Locate every P. falciparum parasite and give its life-cycle stage, and locate every leukocyte and any debris.
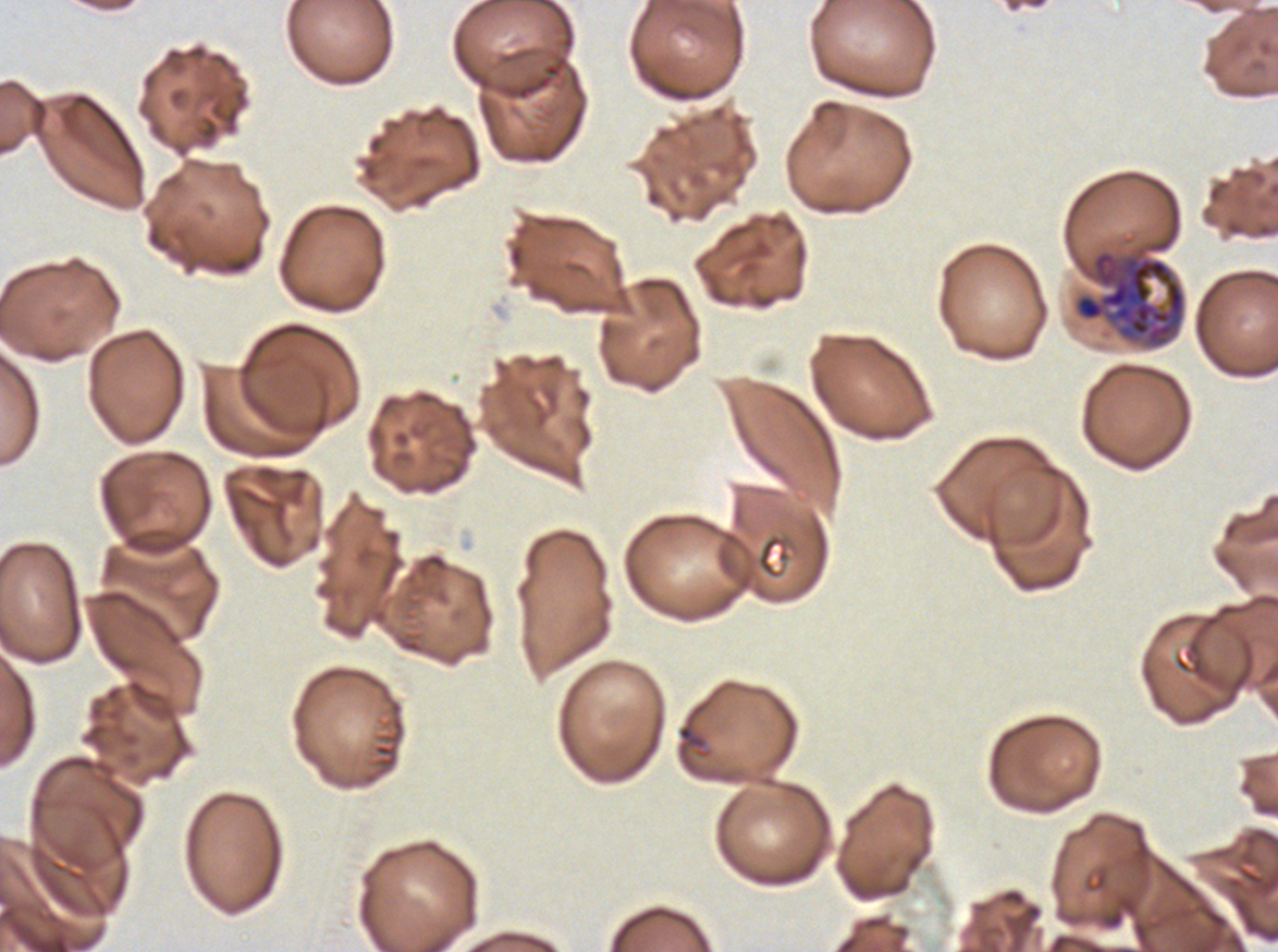

Approximate bounding boxes as [x1, y1, x2, y2] in pixels.
Rings: [677, 723, 707, 751].
Early schizonts: [1074, 250, 1186, 348].
No late-ring/early-trophozoite forms, mid trophozoites, late trophozoites, late schizonts, segmenters, gametocytes, leukocytes, or debris observed.

{
  "image_size": "1278×952 pixels",
  "field_of_view": "one sub-image of a larger composite",
  "stain": "Giemsa",
  "specimen": "P. falciparum from a patient in The Gambia, cultured ex vivo for 24 to 48 hours",
  "preparation": "thin blood smear",
  "life_cycle_stages_observed": "ring, early schizont"
}